State the preparation type.
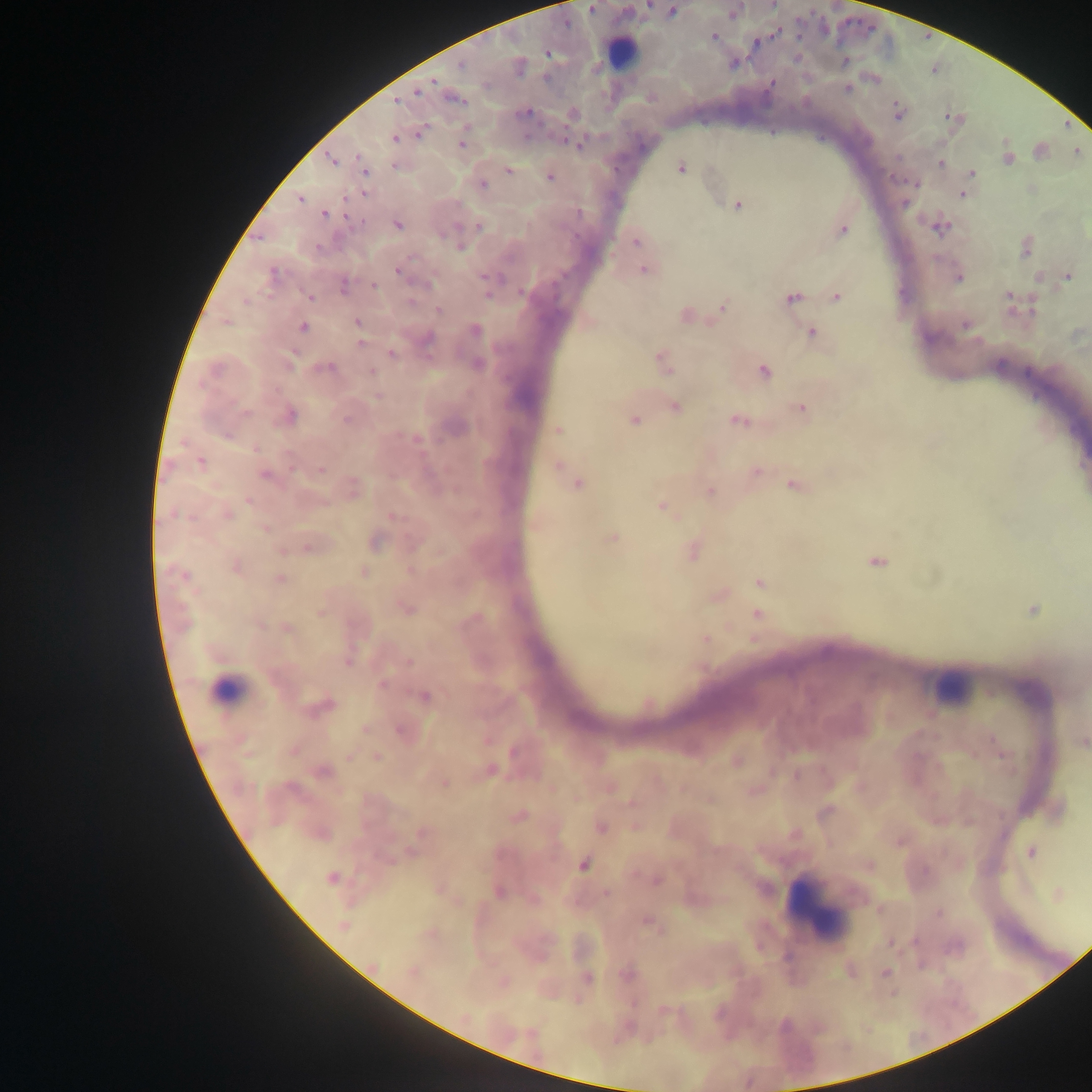

Thick blood smear.

Approximate centers as [x, y] in pixels.
Summary:
  - Leukocyte locations: [620, 53], [225, 689], [951, 689], [815, 903]
  - Malaria parasite locations: [592, 9], [672, 12], [714, 36], [755, 43], [547, 54], [461, 64], [432, 82], [772, 83], [847, 88], [418, 93], [456, 100], [395, 102], [897, 111], [525, 113], [422, 132], [395, 139], [569, 142], [462, 143], [332, 161], [941, 164], [396, 166], [364, 168], [681, 169], [508, 171], [971, 173], [550, 177], [914, 183], [482, 185], [963, 195], [300, 199], [738, 206], [324, 214], [398, 225], [479, 226], [941, 228], [843, 231], [636, 241], [460, 247], [644, 270], [399, 272], [273, 274], [1067, 277], [958, 278], [485, 279], [427, 284], [344, 285], [374, 286], [487, 294], [1010, 296], [310, 297], [837, 297], [792, 298], [722, 307], [439, 310], [358, 322], [966, 326], [303, 327], [476, 330], [811, 333], [427, 339], [360, 343], [392, 354], [290, 363], [478, 364], [664, 364], [327, 369], [764, 370], [372, 372], [378, 396], [675, 408], [801, 409], [289, 416], [347, 420], [635, 420], [738, 421], [558, 430], [200, 462], [556, 465], [321, 471], [757, 471], [265, 475], [578, 485], [793, 487], [710, 492], [249, 500], [662, 506], [228, 515], [393, 516], [265, 528], [613, 538], [375, 542], [309, 547], [877, 562], [237, 567], [364, 572], [184, 575], [280, 579], [759, 583], [407, 609], [1033, 610], [321, 613], [757, 614], [288, 629], [705, 638], [409, 661], [347, 662], [383, 684], [425, 696], [321, 707], [365, 730], [400, 730], [1083, 743], [293, 750], [513, 752], [349, 756], [376, 757], [491, 771], [324, 772], [796, 775], [444, 784], [517, 817], [634, 826], [600, 827], [422, 832], [1031, 852], [584, 865], [331, 878], [658, 880], [498, 892], [606, 893], [939, 913], [649, 924], [344, 926], [890, 942], [413, 971], [885, 973], [627, 974], [588, 978]
  - Image size: 1092×1092 pixels
  - Capture: mobile-phone photograph through a microscope
  - Country: Ghana
  - Field of view: single